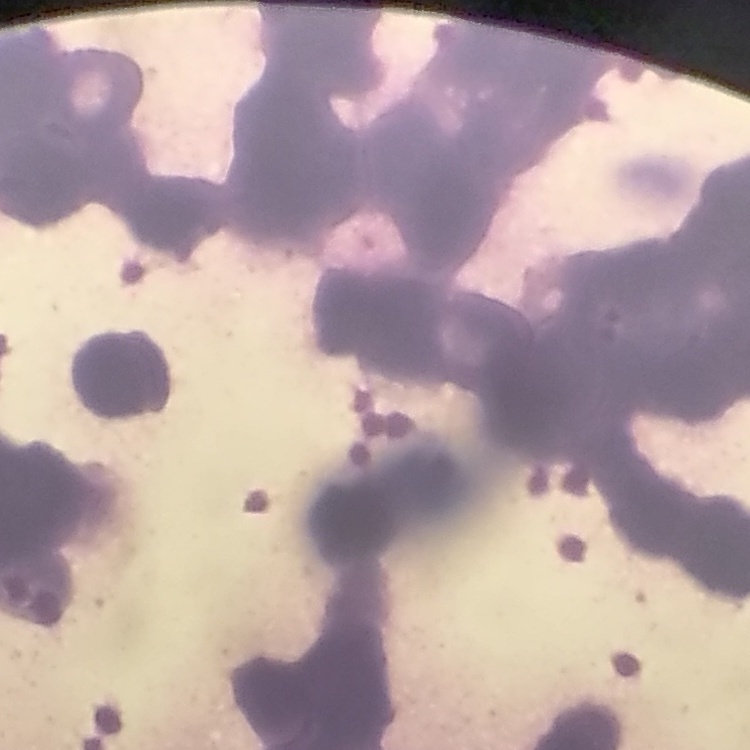
The red blood cells exhibit rouleaux formation. Thin peripheral smear. Square crop of a larger photomicrograph. Stained with either Field's or Giemsa.